Name the parasite shown.
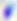
This is Toxoplasma gondii.

Micrograph. 400x magnification.